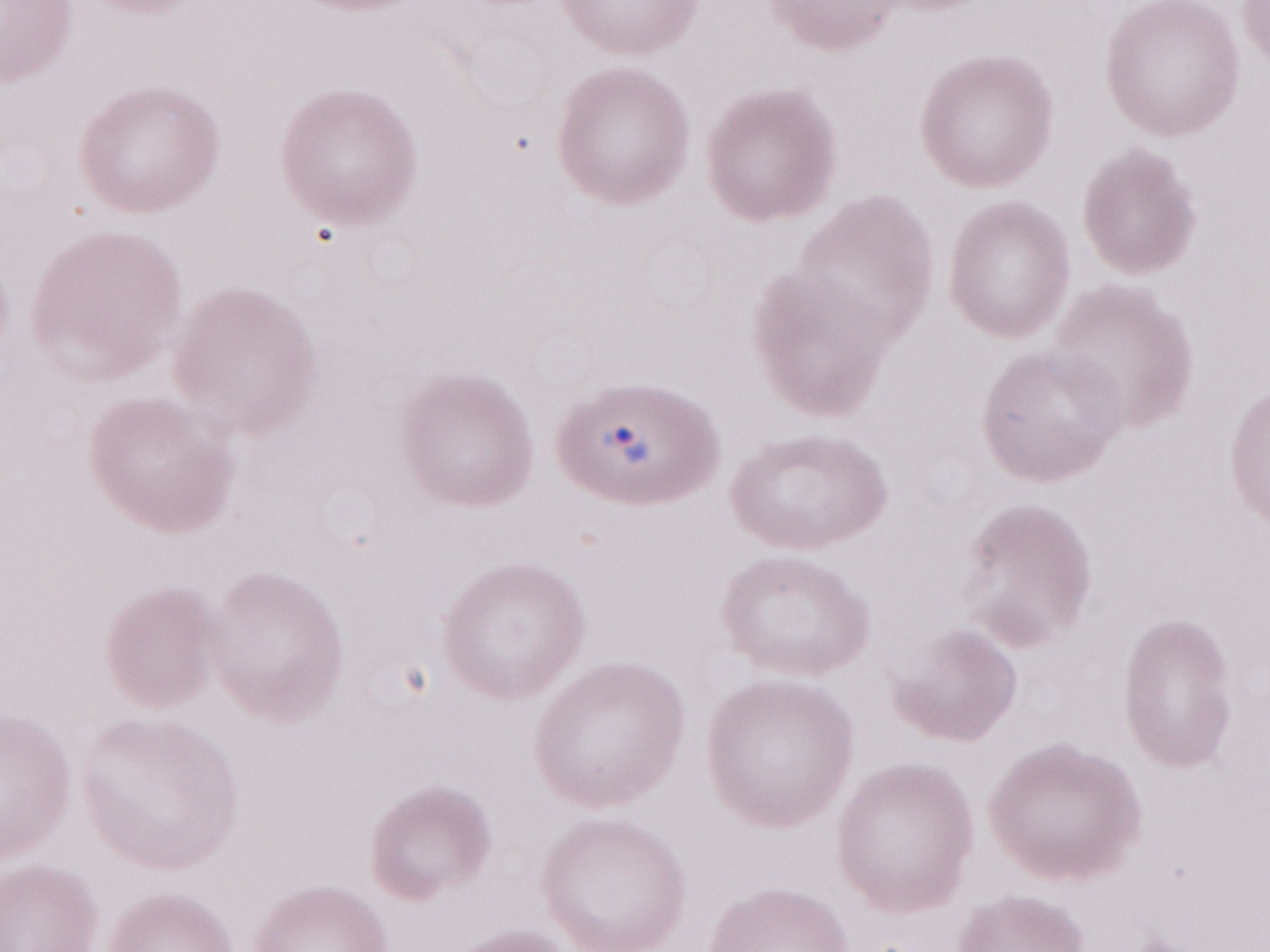

Patient diagnosis: malaria infection. Magnification: 1,000x. One field of this slide. May-Grünwald-Giemsa (MGG) stain. Olympus BX43 microscope, Olympus DP73 camera. Image is 1270×952 pixels. Thin peripheral-blood smear.